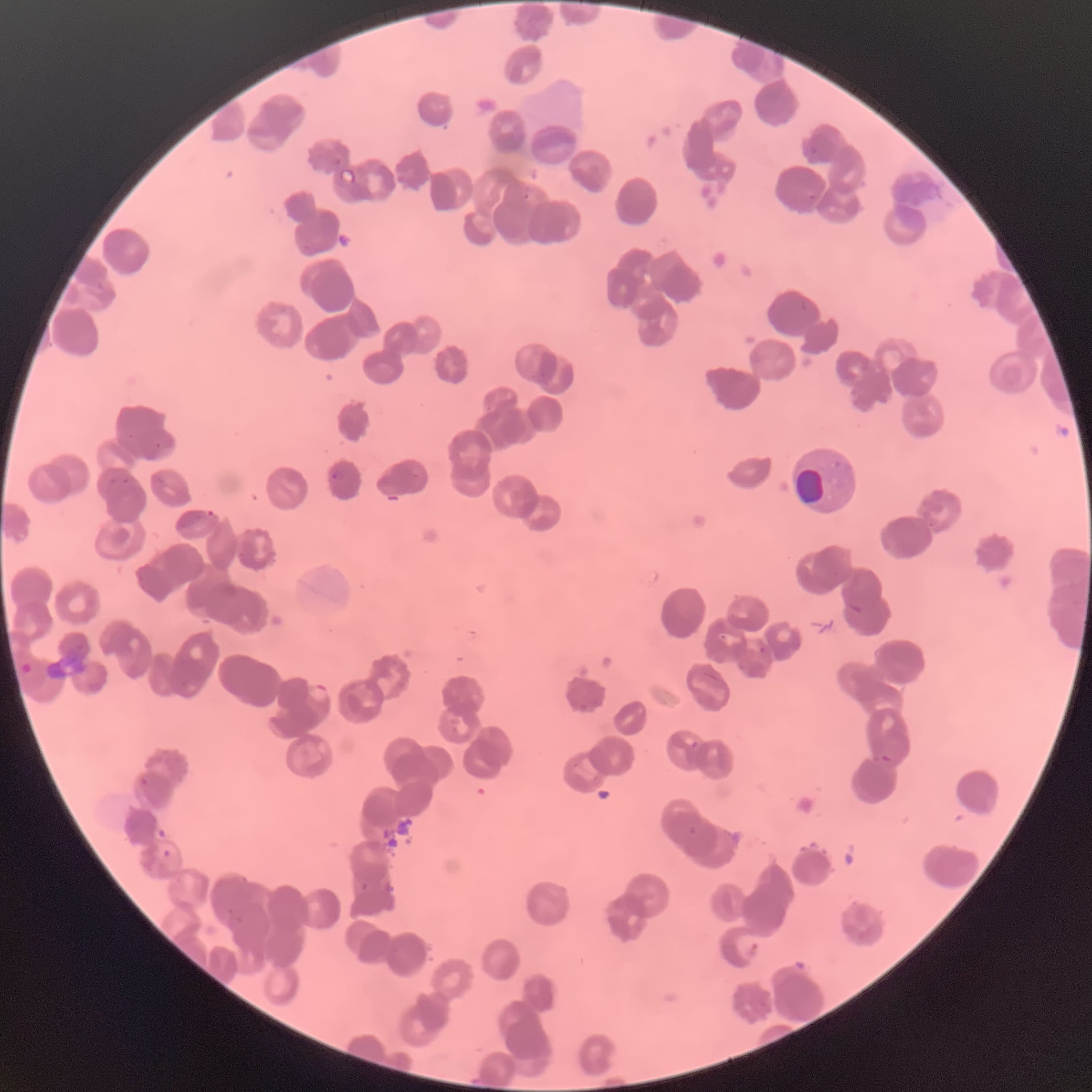 Approximate bounding boxes as (x1,y1)-(x2,y2) corner pairs in pixels. Plasmodium parasite locations: (807,143)-(822,157), (332,156)-(344,166), (338,167)-(358,186), (523,192)-(532,200), (808,193)-(818,202), (302,244)-(313,255), (799,300)-(809,310), (154,441)-(162,449), (331,469)-(345,481), (108,475)-(131,486), (155,475)-(167,486), (202,509)-(216,519), (846,602)-(864,613), (757,645)-(768,654), (306,680)-(331,703), (691,740)-(700,748), (879,754)-(894,764), (140,777)-(148,786), (687,825)-(698,836), (162,850)-(171,858), (360,882)-(371,892). Plasmodium parasites too small for a box (approximate centers as (x,y) in pixels): (131,436). Thin blood film. Image is 1092×1092 pixels. The red blood cells show rouleaux formation. Optical microscopy.